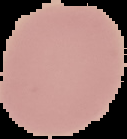

Summary:
  - Preparation: thin blood film
  - Malaria status: uninfected
  - Image type: segmented cell region on a black background
  - Image size: 127×139 pixels